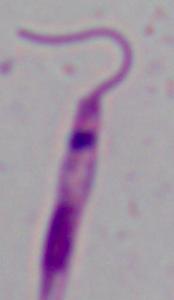

magnification = 1000x
identification = Leishmania
modality = photomicrograph